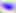

Summary:
  - Magnification: 400x
  - Identification: Toxoplasma gondii
  - Modality: micrograph